Report the malaria status of this cell.
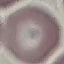

It is uninfected.

Cell patch, automatically extracted from a larger field of view and resized to 64 × 64 pixels. Thin blood film. Giemsa-stained preparation. Acquired by smartphone through the microscope eyepiece.